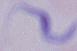
Captured at 1000x magnification. A trypanosome is seen. Micrograph.